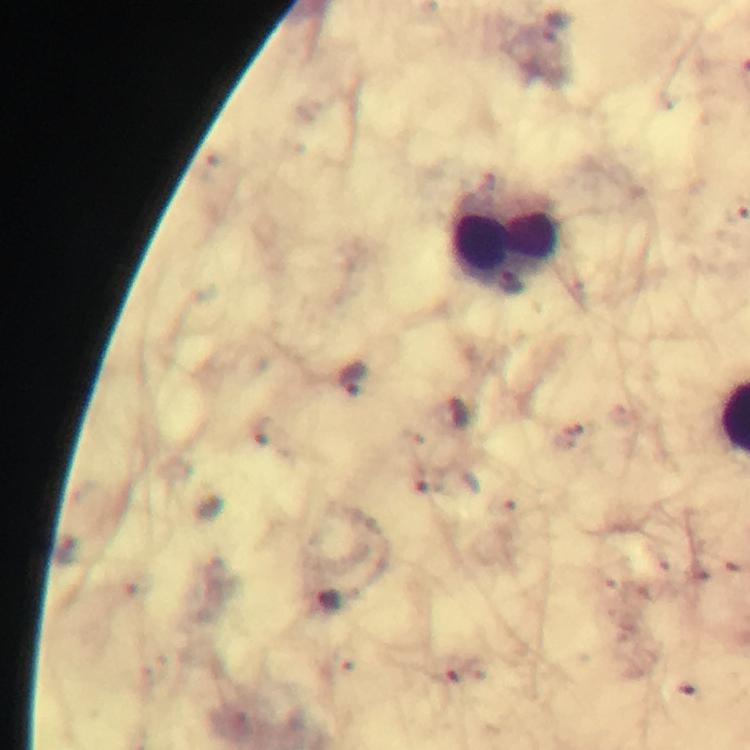
preparation = thick blood film
immersion oil = used
malaria parasite locations = approximate centers as [x, y] in pixels: [352, 378]
leukocyte locations = approximate centers as [x, y] in pixels: [505, 235]
context = from a malaria diagnostic workup
magnification = 100x
image size = 750×750 pixels
cropped from = one field of view
capture = smartphone camera through the microscope
stain = Giemsa